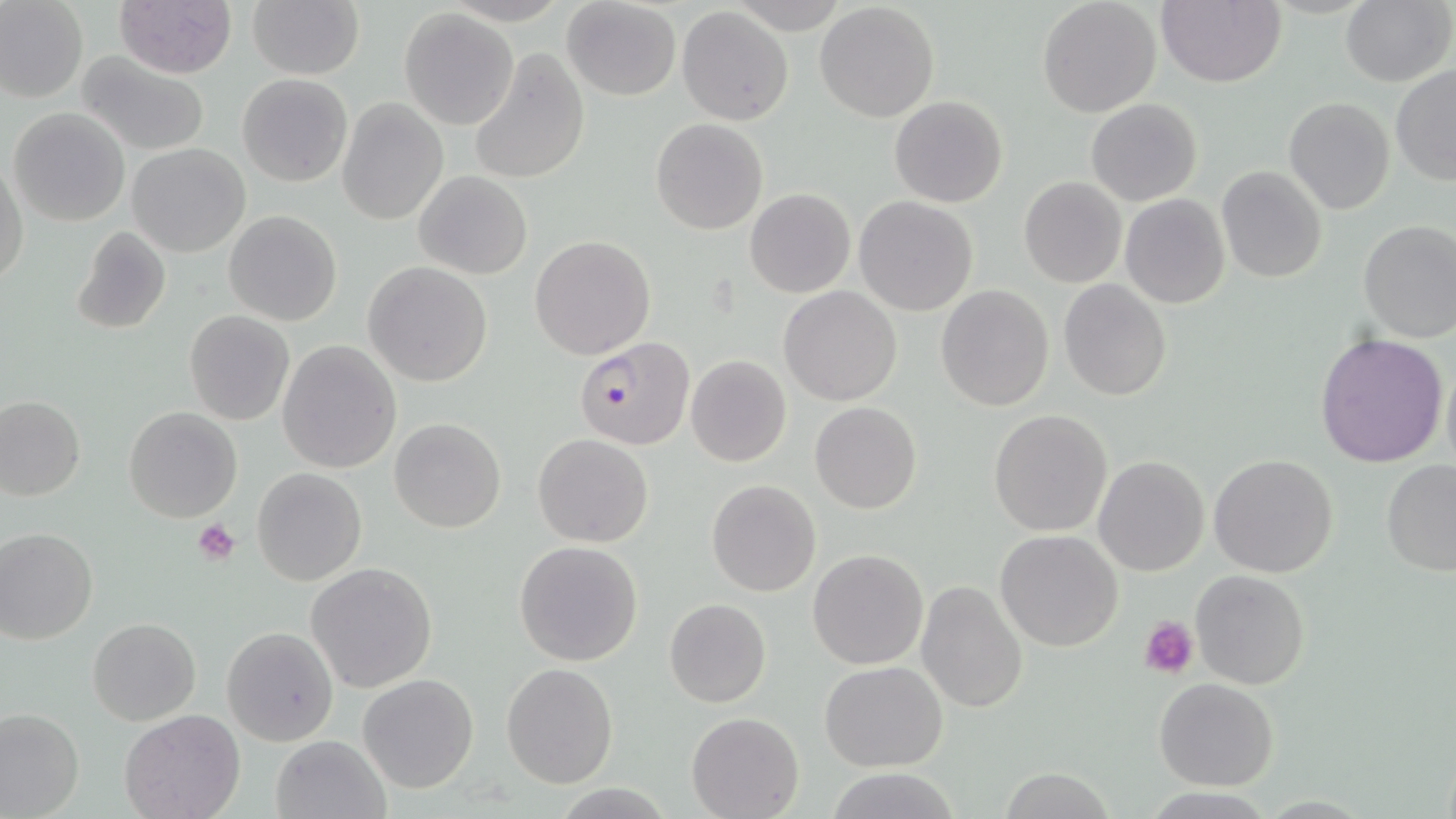

slide_level_diagnosis: Plasmodium falciparum
platelet_locations: 'approximate bounding boxes as [x1, y1, x2, y2] in pixels: [192, 517, 240, 564], [1139, 615, 1198, 679]'
magnification: 1000x
field_of_view: single
preparation: thin blood smear
uninfected_red_blood_cell_locations: 'approximate bounding boxes as [x1, y1, x2, y2] in pixels: [114, 0, 237, 77], [562, 0, 682, 100], [1038, 0, 1161, 117], [1155, 0, 1286, 87], [1340, 0, 1452, 87], [0, 1, 87, 102], [247, 1, 363, 78], [814, 2, 939, 123], [677, 7, 794, 127], [399, 8, 519, 129], [468, 48, 590, 186], [77, 54, 210, 156], [1390, 65, 1456, 186], [237, 74, 353, 188], [889, 95, 1008, 208], [337, 98, 447, 225], [1283, 98, 1396, 217], [1085, 99, 1202, 206], [8, 107, 131, 226], [650, 118, 769, 235], [126, 143, 250, 257], [0, 156, 29, 288], [1216, 165, 1327, 283], [414, 170, 532, 279], [1018, 176, 1128, 288], [744, 187, 855, 297], [1120, 194, 1229, 308], [854, 196, 978, 315], [224, 211, 343, 327], [1357, 220, 1456, 343], [69, 225, 172, 335], [530, 235, 656, 359], [363, 262, 493, 386], [1058, 279, 1172, 402], [935, 284, 1054, 411], [779, 286, 902, 405], [184, 311, 296, 425], [1314, 331, 1450, 470], [277, 340, 402, 473], [685, 356, 793, 468], [1440, 357, 1455, 483], [0, 397, 85, 502], [810, 401, 922, 513], [123, 407, 243, 523], [987, 408, 1113, 538], [390, 417, 506, 532], [533, 433, 653, 546], [1208, 453, 1339, 578], [1094, 455, 1210, 576], [1381, 460, 1456, 578], [251, 467, 368, 586], [706, 479, 822, 597], [0, 527, 98, 644], [994, 530, 1123, 652], [513, 541, 644, 667], [807, 548, 929, 669], [306, 560, 439, 694], [1190, 569, 1312, 691], [917, 580, 1029, 717], [664, 598, 771, 707], [87, 616, 201, 725], [222, 627, 339, 746], [820, 661, 949, 769], [501, 663, 618, 788], [358, 674, 479, 793], [1153, 678, 1279, 790], [0, 707, 83, 819], [119, 711, 245, 819], [686, 712, 803, 819], [269, 733, 392, 819], [1000, 768, 1116, 818]'
plasmodium_falciparum_infected_red_blood_cell_locations: 'approximate bounding boxes as [x1, y1, x2, y2] in pixels: [573, 338, 693, 450]'
modality: light microscopy
stain: May-Grünwald-Giemsa
image_size: 1456×819 pixels